Report the malaria status of this cell.
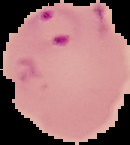

It is parasitized.

image size = 130×145 pixels
image type = cell region segmented out of the field of view; surrounding area masked to black
preparation = thin blood film